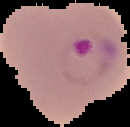
image type = cell region segmented out of the field of view; surrounding area masked to black
malaria status = parasitized
preparation = thin blood smear
image size = 130×127 pixels